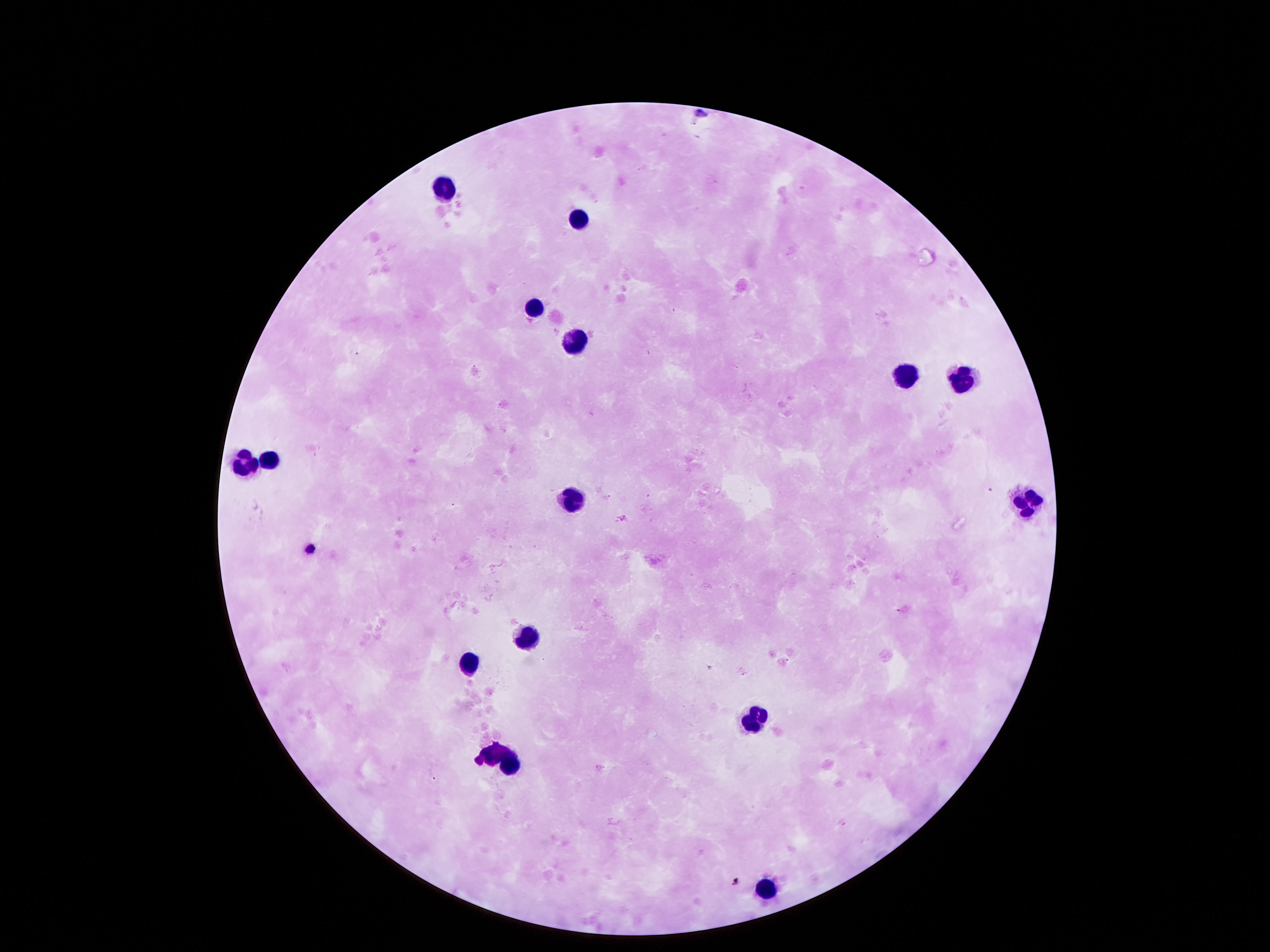

field of view = one from this slide
image size = 1270×952 pixels
stain = Giemsa
magnification = 100x
preparation = thick peripheral-blood smear
capture = smartphone camera through the microscope eyepiece
leukocyte locations = approximate object centers, in pixels from the top-left corner: (x=445, y=189), (x=582, y=217), (x=536, y=303), (x=575, y=340), (x=903, y=379), (x=962, y=380), (x=268, y=456), (x=246, y=466), (x=575, y=502), (x=1026, y=504), (x=527, y=633), (x=464, y=661), (x=757, y=720), (x=502, y=760), (x=762, y=887)
patient malaria status = uninfected